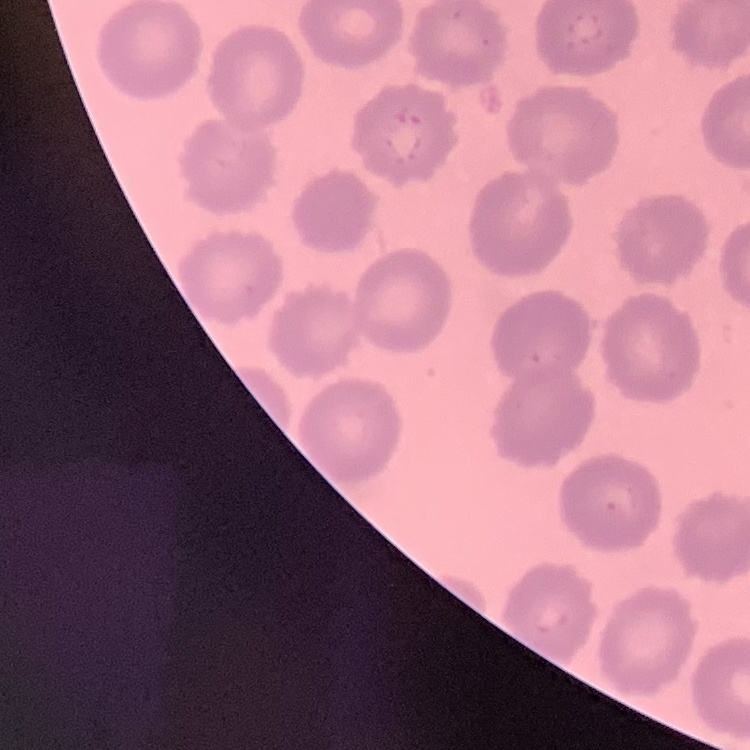
Summary:
  - Red blood cell morphology: no rouleaux formation
  - Image type: one tile cut from a larger photomicrograph
  - Preparation: thin peripheral smear
  - Stain: Field's or Giemsa